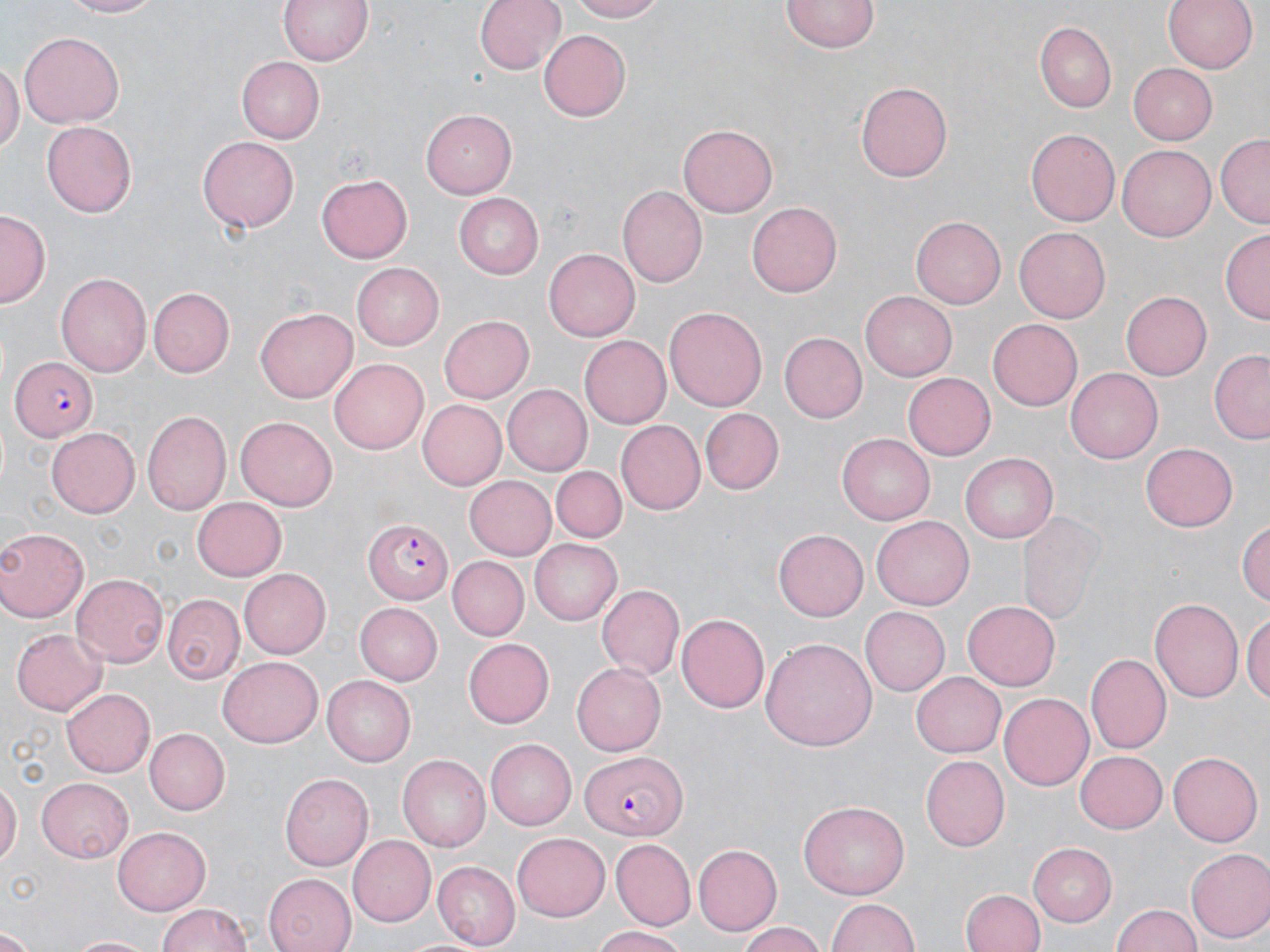
Approximate bounding boxes as (x1,y1)-(x2,y2) corner pairs in pixels. Uninfected red blood cell locations: (55,0)-(164,17), (276,0)-(377,67), (475,0)-(562,75), (565,0)-(666,22), (1164,0)-(1259,74), (781,1)-(877,54), (1035,21)-(1117,111), (19,30)-(123,124), (538,30)-(630,121), (236,57)-(326,143), (0,60)-(21,156), (1125,62)-(1217,146), (858,79)-(955,181), (421,110)-(517,199), (42,122)-(137,216), (677,125)-(778,218), (1026,130)-(1118,227), (1215,133)-(1270,227), (198,136)-(298,233), (1118,145)-(1216,241), (317,174)-(413,263), (616,185)-(707,289), (453,191)-(545,276), (746,202)-(843,297), (0,211)-(49,306), (911,215)-(1006,309), (1016,226)-(1112,323), (1220,229)-(1269,324), (545,249)-(639,340), (354,261)-(447,350), (56,270)-(152,380), (150,287)-(235,377), (861,290)-(957,381), (1120,290)-(1212,380), (666,304)-(768,411), (256,308)-(358,402), (437,315)-(533,404), (988,318)-(1083,409), (779,332)-(867,422), (581,335)-(671,428), (1208,349)-(1270,444), (329,358)-(431,455), (1066,368)-(1163,464), (903,372)-(996,459), (502,384)-(592,474), (418,400)-(507,489), (699,408)-(783,495), (142,410)-(232,515), (235,417)-(338,512), (614,421)-(704,516), (46,427)-(141,518), (838,433)-(937,524), (1140,442)-(1239,531), (961,453)-(1057,542), (553,467)-(625,542), (464,475)-(559,561), (193,497)-(288,581), (871,516)-(973,610), (1240,517)-(1270,608), (0,527)-(89,621), (774,529)-(868,620), (530,539)-(622,624), (446,557)-(527,640), (238,566)-(331,659), (72,571)-(167,665), (597,584)-(684,678), (164,595)-(242,683), (1151,596)-(1244,703), (962,600)-(1060,690), (357,602)-(442,684), (860,607)-(949,694), (675,611)-(768,711), (1243,611)-(1270,708), (11,628)-(106,715), (761,638)-(876,755), (464,639)-(555,727), (1087,655)-(1170,752), (218,657)-(323,748), (573,662)-(667,756), (912,672)-(1006,757), (323,677)-(414,766), (62,689)-(154,777), (999,693)-(1098,790), (143,726)-(230,816), (485,740)-(576,830), (1073,750)-(1166,834), (1169,751)-(1262,845), (399,754)-(494,852), (920,754)-(1010,851), (280,773)-(371,871), (38,777)-(135,860), (0,779)-(20,871), (800,801)-(911,901), (111,826)-(212,914), (513,833)-(611,920), (347,836)-(434,926), (612,839)-(697,927), (1028,842)-(1116,925), (692,843)-(781,935), (1186,849)-(1270,944), (433,862)-(520,948), (263,873)-(358,952), (961,888)-(1045,952), (828,897)-(920,952), (155,903)-(255,952), (1109,905)-(1204,952), (737,924)-(829,952), (592,926)-(694,951), (0,931)-(34,951), (403,934)-(489,952), (67,935)-(153,951). Plasmodium falciparum-infected red blood cell locations: (8,354)-(99,441), (364,518)-(452,604), (581,750)-(683,838). Slide-level diagnosis: Plasmodium falciparum. Image is 1270×952 pixels. Thin blood smear. May-Grünwald-Giemsa stain. 1000x magnification. One field of a larger specimen. Optical microscopy.